Describe the morphology of the red blood cells.
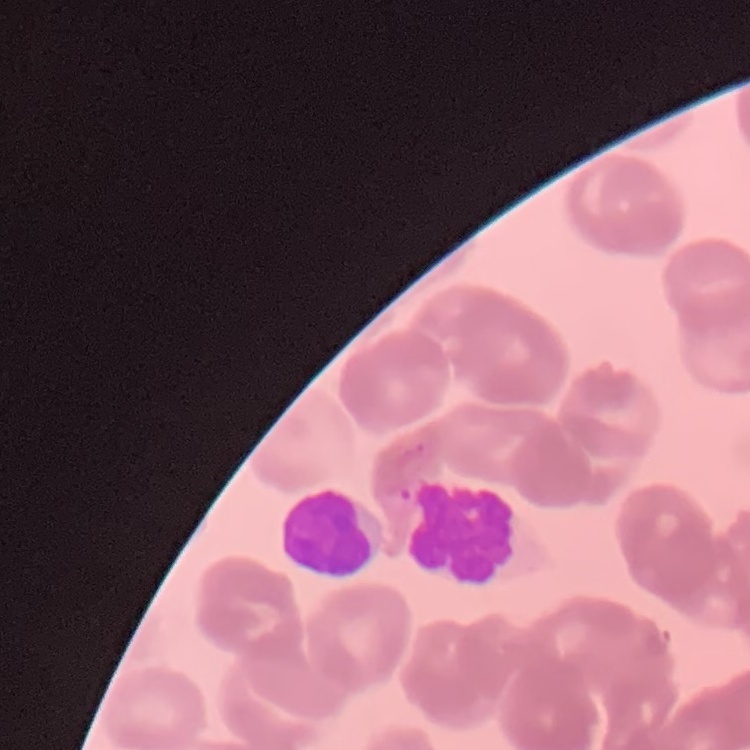
Rouleaux formation.

Summary:
  - Preparation: thin peripheral smear
  - Stain: Field's or Giemsa
  - Image type: square crop of a larger photomicrograph